Classify this cell by malaria status.
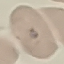
It is uninfected.

{
  "preparation": "thin blood smear",
  "capture": "smartphone through the microscope eyepiece",
  "stain": "Giemsa",
  "image_type": "automatically extracted cell patch, resized to 64 × 64 pixels"
}